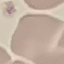

Result: negative for malaria parasites. Thin blood film. Automatically extracted cell patch, resized to 64 × 64 pixels. Photographed with a smartphone camera at the microscope eyepiece. Giemsa stain.